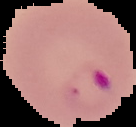

{
  "result": "Plasmodium parasites identified",
  "preparation": "thin blood smear",
  "image_size": "136×127 pixels",
  "image_type": "cell region segmented out of the field of view; surrounding area masked to black"
}